Name the cell type shown.
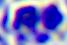

A leukocyte.

Summary:
  - Modality: micrograph
  - Magnification: 400x